State the preparation type.
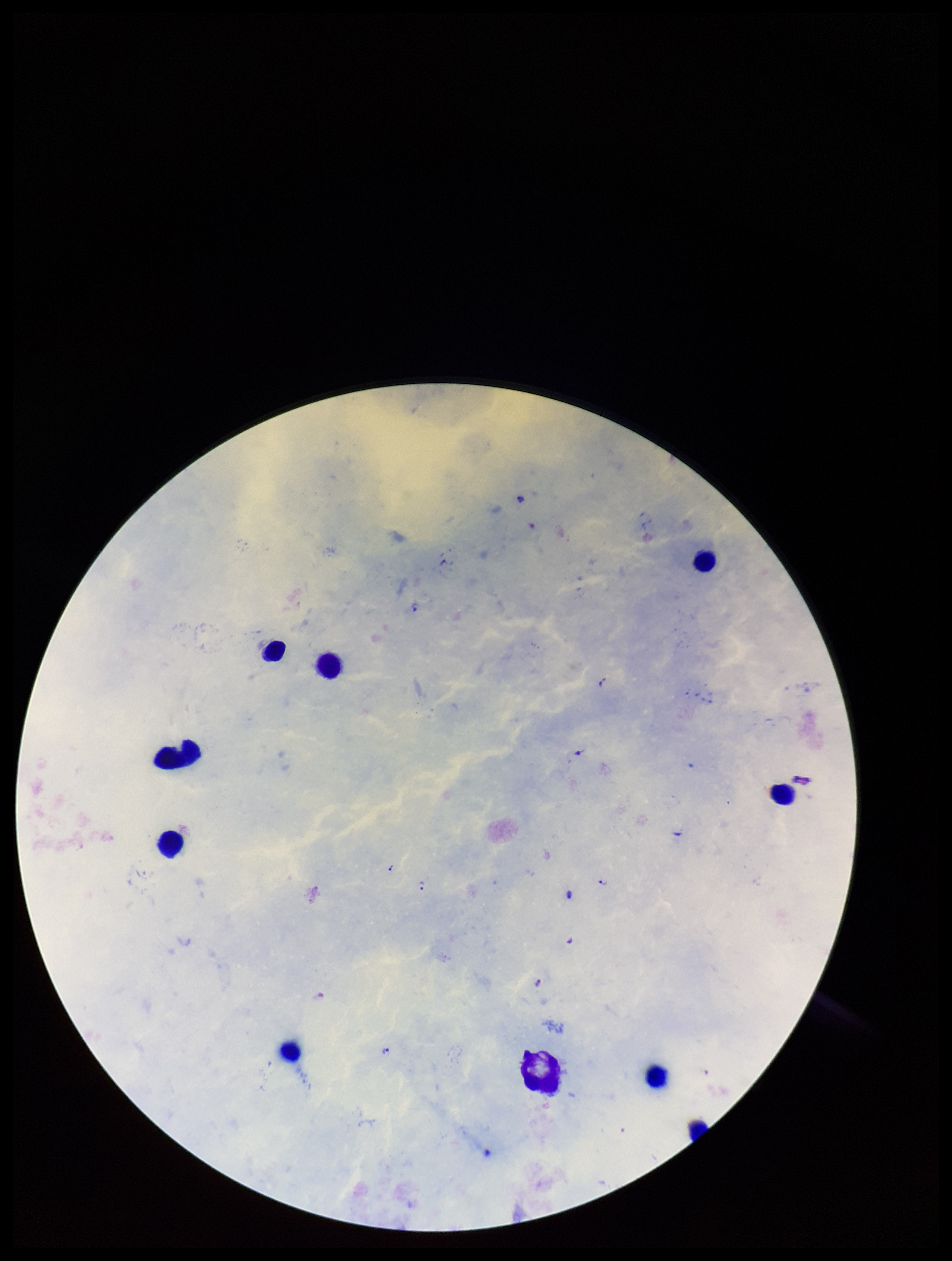

Thick.

parasite count = 10
capture = smartphone photograph through the microscope eyepiece
field of view = single
leukocyte count = 10
stain = Giemsa
species reported for this patient = Plasmodium falciparum
Plasmodium parasites = detected
image size = 952×1261 pixels
patient malaria status = infected